Classify this cell by malaria status.
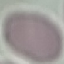
Uninfected.

Cell patch, automatically extracted from a larger field of view and resized to 64 × 64 pixels. Giemsa-stained preparation. Photographed with a smartphone camera at the microscope eyepiece. Thin blood smear.